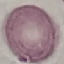

Summary:
  - Result: no malaria parasites seen
  - Image type: automatically extracted cell patch, resized to 64 × 64 pixels
  - Stain: Giemsa
  - Capture: smartphone through the microscope eyepiece
  - Preparation: thin blood smear